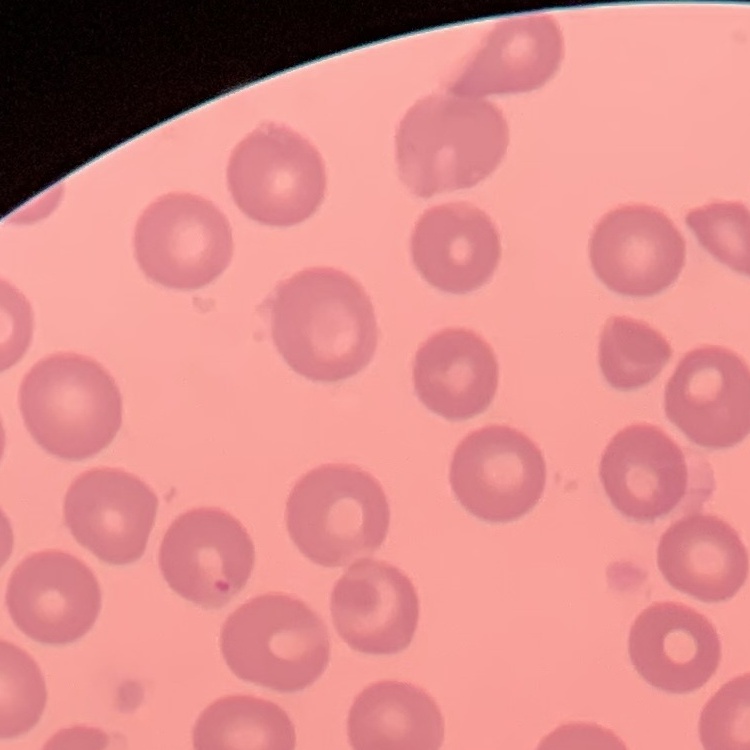
The red blood cells exhibit no rouleaux formation. Thin blood film. Field's or Giemsa stain. One tile cut from a larger photomicrograph.